Locate every blood parasite and identify its species.
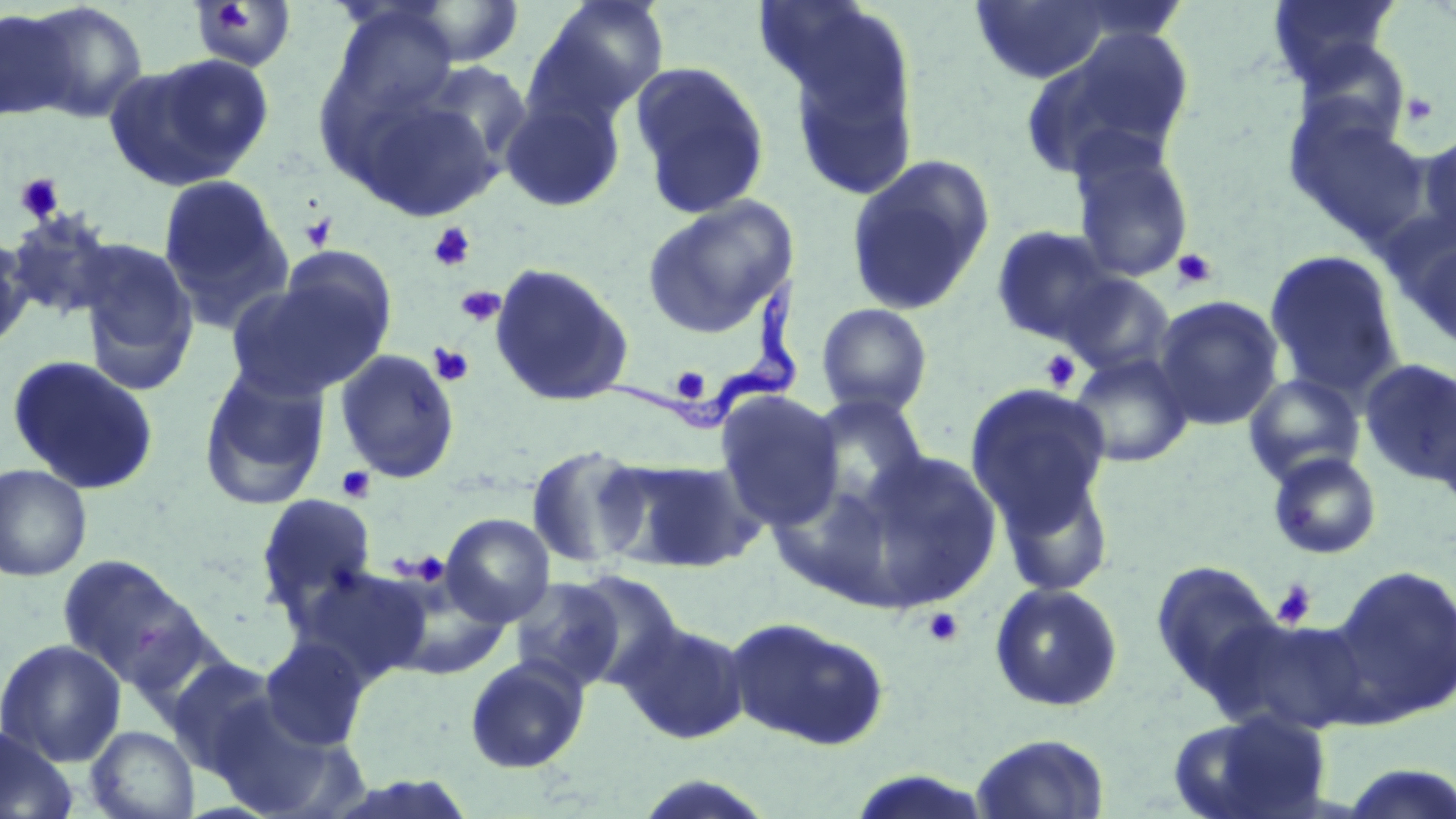

Approximate bounding boxes as (x1, y1, x2, y2) in pixels.
Trypanosoma brucei: (593, 275, 805, 433).
No Plasmodium falciparum, Plasmodium ovale, Plasmodium malariae, Plasmodium vivax, or Babesia divergens observed.

slide-level diagnosis = Trypanosoma brucei
field of view = one of a larger specimen
platelet locations = approximate bounding boxes as (x1, y1, x2, y2) in pixels: (1401, 92, 1438, 126), (15, 173, 65, 223), (298, 213, 337, 251), (428, 222, 475, 271), (1171, 247, 1218, 291), (455, 286, 505, 326), (429, 343, 474, 386), (1039, 349, 1080, 392), (669, 366, 712, 404), (335, 466, 376, 503), (406, 551, 450, 586), (1272, 579, 1316, 628), (923, 607, 964, 646)
stain = May-Grünwald-Giemsa
uninfected red blood cell locations = approximate bounding boxes as (x1, y1, x2, y2) in pixels: (1266, 0, 1402, 87), (527, 1, 670, 127), (970, 1, 1119, 85), (21, 2, 149, 123), (185, 2, 299, 73), (397, 3, 527, 68), (764, 7, 924, 205), (0, 8, 76, 122), (1019, 26, 1196, 182), (1290, 37, 1412, 150), (107, 53, 274, 189), (628, 60, 772, 219), (499, 93, 626, 212), (1286, 109, 1431, 246), (1416, 130, 1456, 244), (1069, 136, 1195, 283), (844, 154, 996, 316), (157, 174, 293, 327), (641, 196, 797, 337), (5, 209, 119, 321), (990, 225, 1122, 345), (1403, 229, 1456, 354), (0, 234, 34, 349), (75, 238, 200, 393), (1264, 249, 1405, 400), (489, 262, 633, 407), (225, 271, 388, 401), (1056, 272, 1176, 378), (1152, 295, 1285, 431), (816, 303, 933, 418), (334, 349, 460, 483), (1068, 353, 1194, 468), (6, 354, 160, 495), (1359, 358, 1456, 488), (198, 365, 330, 511), (1242, 372, 1366, 486), (964, 383, 1112, 535), (715, 390, 845, 531), (805, 394, 931, 517), (525, 444, 650, 571), (845, 448, 1000, 609), (1267, 451, 1382, 560), (602, 456, 762, 573), (992, 458, 1116, 600), (0, 463, 92, 582), (255, 493, 378, 621), (440, 513, 555, 627), (56, 553, 214, 697), (1150, 560, 1282, 701), (292, 564, 433, 686), (1325, 564, 1456, 725), (378, 570, 514, 680), (567, 570, 687, 690), (508, 577, 628, 693), (988, 582, 1124, 712), (725, 616, 890, 750), (1211, 616, 1369, 733), (618, 619, 751, 744), (0, 638, 126, 767), (258, 638, 371, 751), (464, 656, 590, 774), (164, 657, 286, 776), (208, 696, 360, 818), (1170, 709, 1333, 819), (86, 726, 199, 818), (0, 727, 78, 819), (970, 733, 1110, 818), (1335, 762, 1456, 818), (629, 774, 779, 818)
magnification = 1000x
image size = 1456×819 pixels
modality = optical microscopy
preparation = thin blood film